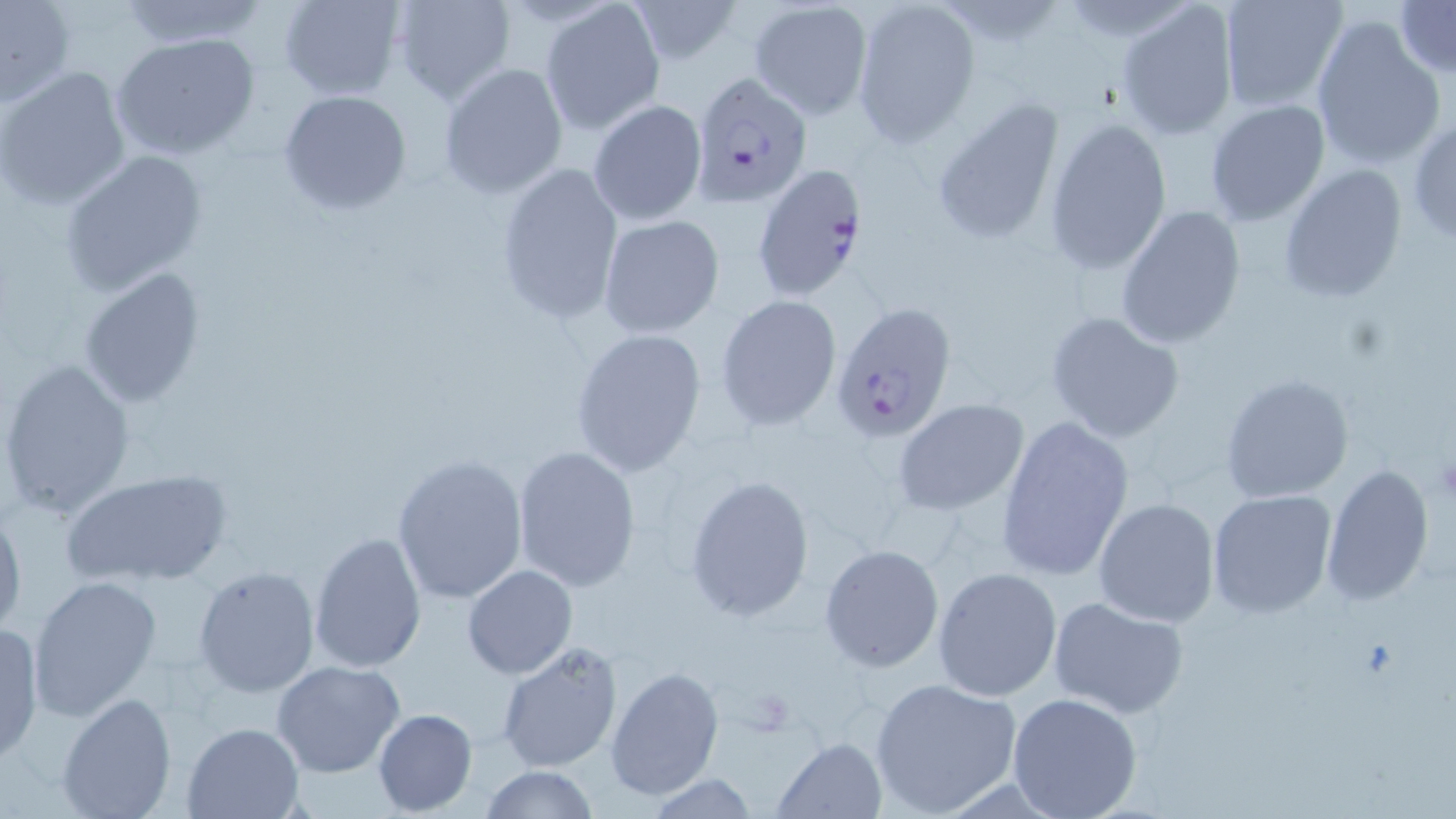

{
  "slide_level_diagnosis": "Plasmodium falciparum",
  "uninfected_red_blood_cell_locations": "approximate bounding boxes as [x1, y1, x2, y2] in pixels: [278, 0, 406, 101], [392, 0, 516, 106], [627, 0, 743, 66], [1116, 0, 1240, 140], [1215, 0, 1349, 111], [112, 1, 268, 49], [747, 1, 872, 121], [851, 1, 981, 146], [1395, 1, 1455, 76], [0, 2, 74, 106], [540, 2, 665, 134], [1309, 15, 1446, 169], [110, 33, 261, 160], [437, 63, 569, 199], [0, 66, 132, 210], [277, 89, 413, 215], [930, 98, 1066, 248], [589, 100, 707, 225], [1204, 100, 1330, 226], [1407, 116, 1456, 241], [1045, 117, 1172, 274], [59, 150, 210, 296], [495, 161, 625, 322], [1278, 164, 1407, 303], [1115, 203, 1246, 347], [598, 215, 725, 339], [78, 266, 206, 408], [716, 295, 841, 431], [1044, 310, 1186, 443], [571, 327, 708, 478], [0, 358, 134, 520], [1220, 373, 1354, 503], [895, 399, 1029, 517], [997, 419, 1136, 579], [512, 446, 641, 593], [391, 454, 530, 607], [1320, 464, 1433, 605], [59, 466, 235, 588], [684, 473, 817, 621], [1206, 489, 1336, 619], [1093, 498, 1220, 627], [0, 503, 26, 640], [309, 529, 427, 674], [819, 544, 944, 671], [463, 564, 577, 678], [193, 565, 320, 698], [932, 566, 1062, 702], [28, 575, 162, 721], [1048, 596, 1189, 719], [0, 621, 45, 765], [495, 643, 623, 773], [270, 660, 406, 778], [604, 664, 724, 800], [869, 675, 1025, 818], [58, 691, 176, 819], [1007, 692, 1144, 819], [372, 707, 477, 815], [183, 720, 304, 818], [773, 736, 885, 817], [477, 766, 601, 819], [645, 775, 762, 817]",
  "preparation": "thin blood film",
  "field_of_view": "one of a larger specimen",
  "magnification": "1000x",
  "modality": "light microscopy",
  "platelet_locations": "approximate bounding boxes as [x1, y1, x2, y2] in pixels: [1434, 449, 1456, 506]",
  "image_size": "1456×819 pixels",
  "stain": "May-Grünwald-Giemsa",
  "plasmodium_falciparum_infected_red_blood_cell_locations": "approximate bounding boxes as [x1, y1, x2, y2] in pixels: [689, 71, 813, 208], [751, 165, 870, 299], [831, 300, 957, 444]"
}